Assess this cell for malaria.
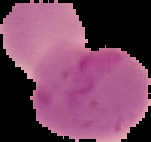

It is parasitized.

Summary:
  - Image type: cell region segmented out of the field of view; surrounding area masked to black
  - Preparation: thin blood film
  - Image size: 151×142 pixels